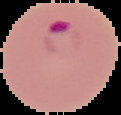

The area outside the segmented cell region is set to black. Malaria status: parasitized. Image is 121×115 pixels. From a thin blood film.